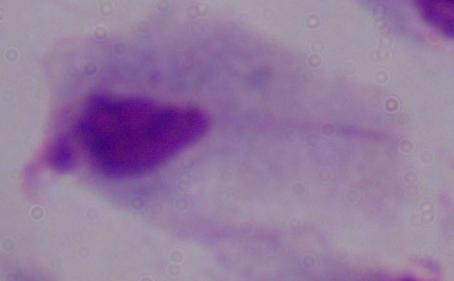

{
  "modality": "micrograph",
  "identification": "trichomonad",
  "magnification": "1000x"
}